Assess for Plasmodium parasites.
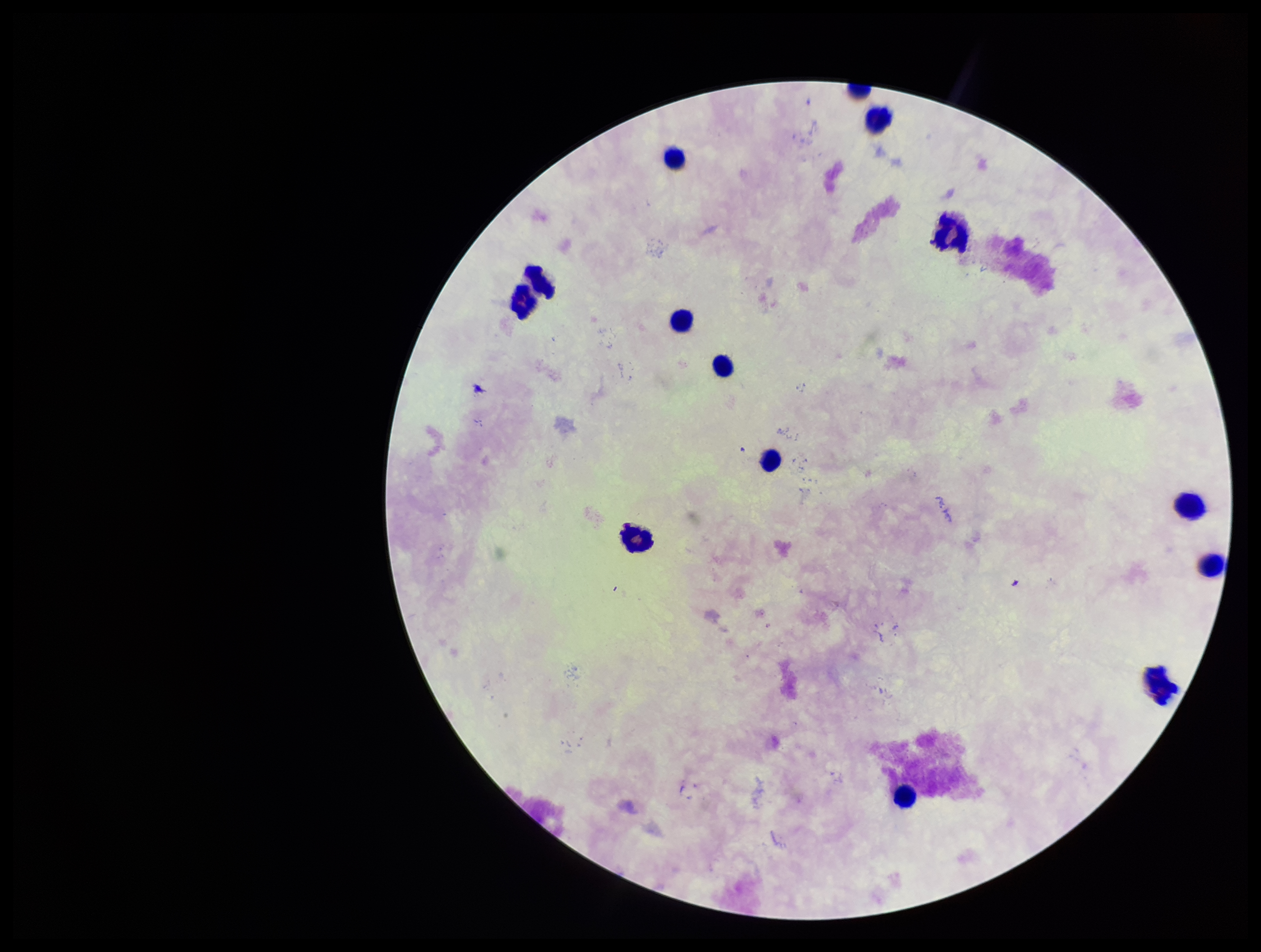

None identified.

patient malaria status = negative
capture = smartphone photograph through the microscope eyepiece
parasite count = 0
stain = Giemsa
leukocyte count = 14
field of view = single
preparation = thick smear
image size = 1261×952 pixels